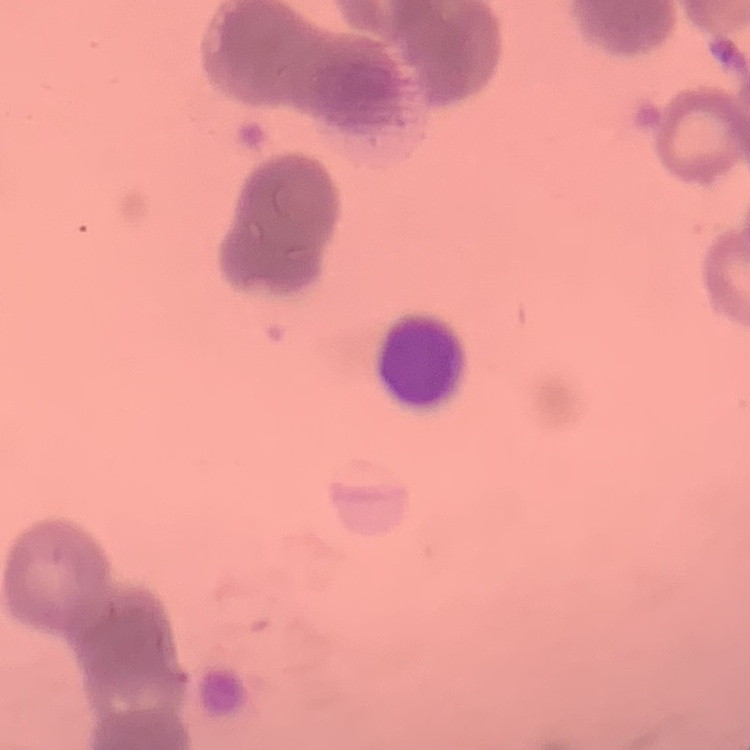

Summary:
  - Red blood cell morphology: rouleaux formation
  - Stain: Field's or Giemsa
  - Image type: square crop of a larger photomicrograph
  - Preparation: thin blood film